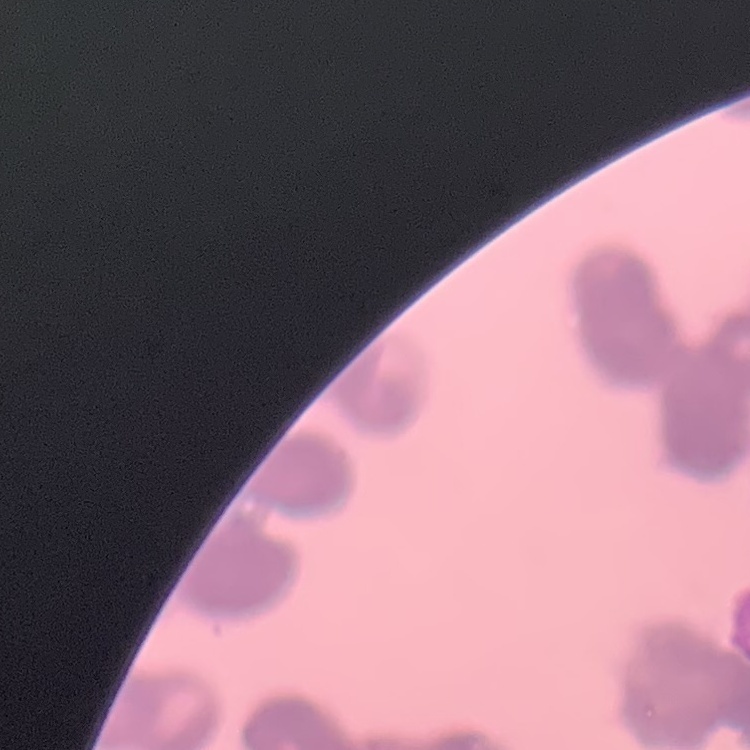

Summary:
  - Red blood cell morphology: rouleaux formation
  - Image type: one tile cut from a larger photomicrograph
  - Preparation: thin blood smear
  - Stain: Field's or Giemsa